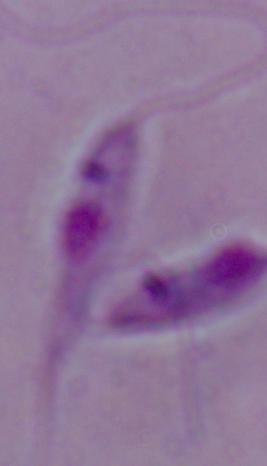

Micrograph. A Leishmania parasite is seen. 1000x magnification.